Assess this cell for malaria.
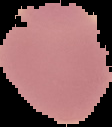
It is uninfected.

Summary:
  - Preparation: thin blood film
  - Image type: segmented cell region with the area outside set to black
  - Image size: 112×127 pixels